Assess the morphology of the red blood cells.
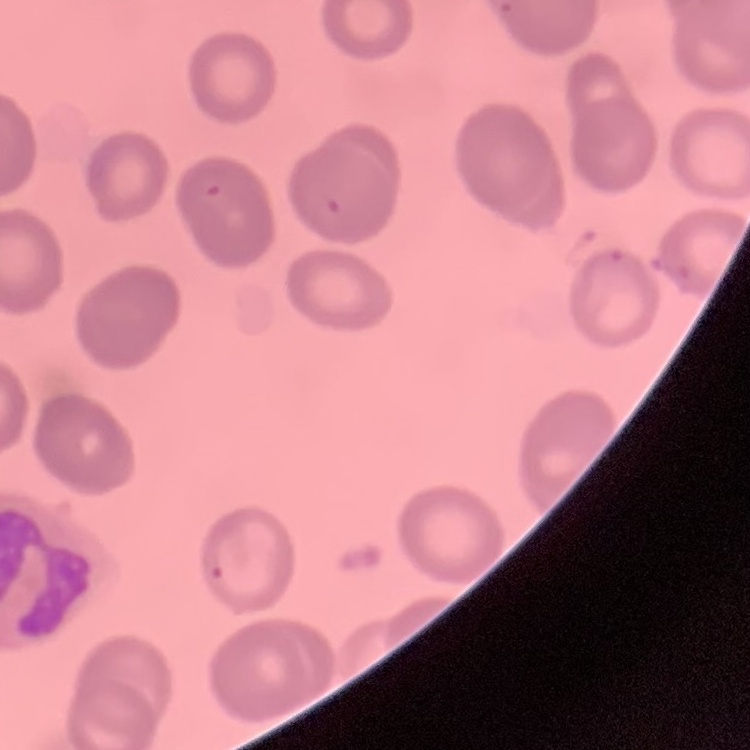

They show no rouleaux formation.

Summary:
  - Image type: square crop of a larger photomicrograph
  - Stain: Field's or Giemsa
  - Preparation: thin blood film